Describe the morphology of the red blood cells.
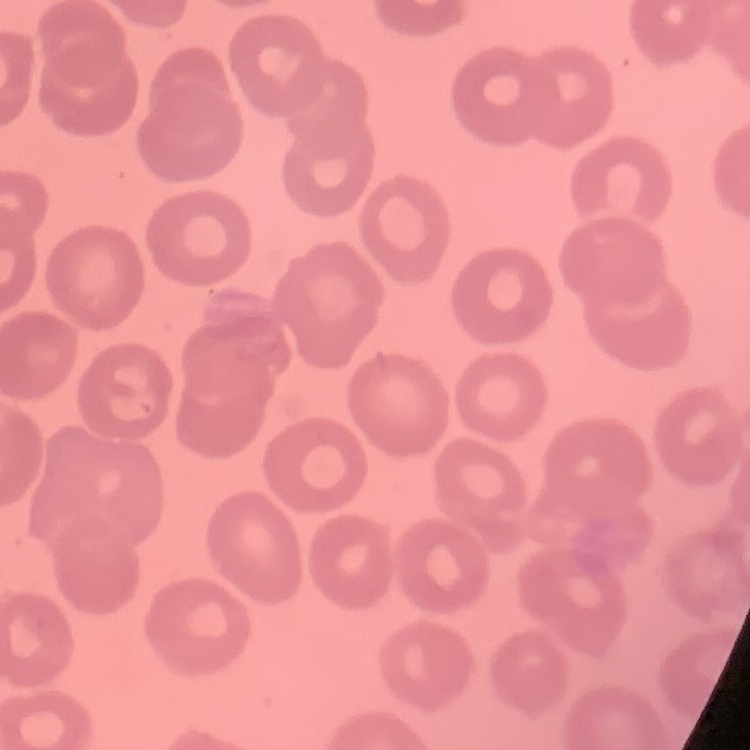
No rouleaux formation.

image type = square crop of a larger photomicrograph
preparation = thin blood smear
stain = Field's or Giemsa